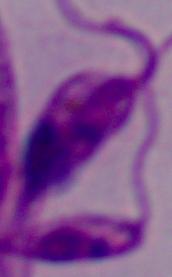
Photomicrograph. Captured at 1000x magnification. A Leishmania parasite is shown.